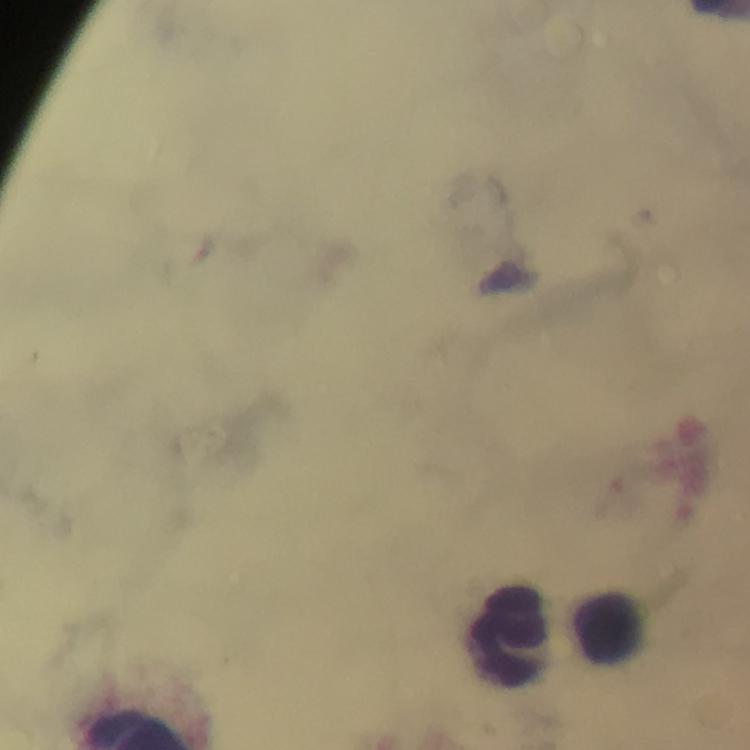
{
  "stain": "Giemsa",
  "preparation": "thick blood smear",
  "cropped_from": "a single field of view",
  "immersion_oil": "used",
  "image_size": "750×750 pixels",
  "context": "from a diagnostic examination for malaria",
  "magnification": "100x",
  "leukocyte_locations": "approximate centers as [x, y] in pixels: [609, 629], [514, 637]",
  "capture": "smartphone camera through the microscope",
  "plasmodium_parasites": "none seen"
}